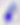
magnification = 400x
modality = photomicrograph
identification = Toxoplasma gondii